State the blood parasite species.
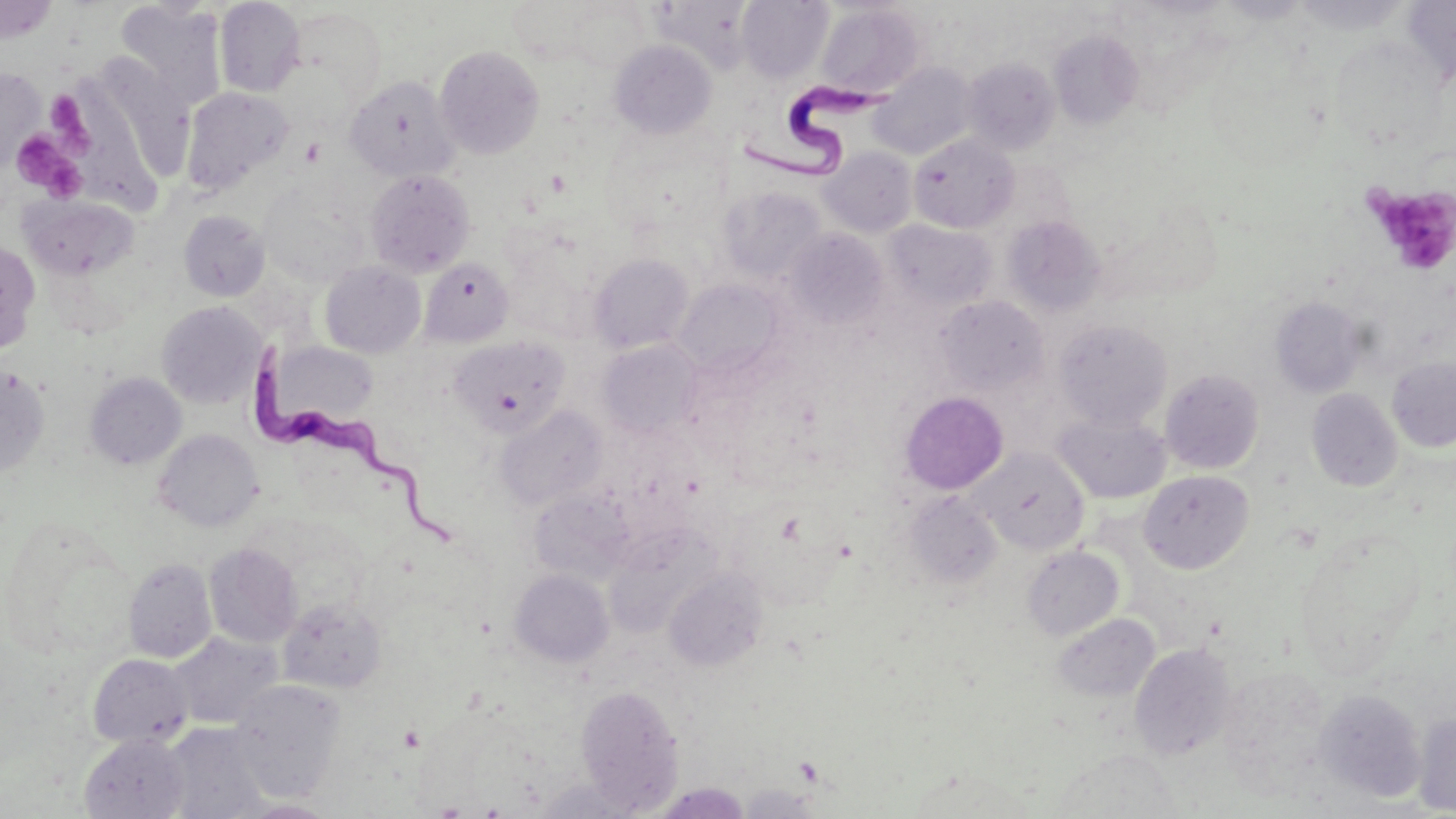

Trypanosoma brucei.

uninfected red blood cell locations = approximate bounding boxes as (x1,y1)-(x2,y2) corner pairs in pixels: (214,0)-(306,97), (737,0)-(833,82), (1292,0)-(1412,35), (1400,0)-(1456,85), (115,1)-(226,104), (1,2)-(58,43), (566,3)-(651,73), (815,3)-(925,99), (286,6)-(385,104), (1048,29)-(1143,130), (1330,36)-(1447,149), (609,40)-(717,140), (435,45)-(545,160), (964,58)-(1060,155), (870,63)-(976,160), (0,67)-(45,171), (343,75)-(462,183), (180,87)-(294,195), (909,133)-(1019,233), (819,147)-(917,238), (365,169)-(475,277), (259,186)-(370,287), (717,186)-(826,285), (20,195)-(140,280), (178,210)-(271,301), (1002,215)-(1105,315), (883,220)-(995,315), (785,229)-(889,329), (0,239)-(41,354), (501,250)-(592,343), (589,253)-(694,353), (419,257)-(514,346), (320,261)-(426,358), (673,278)-(786,379), (934,295)-(1049,396), (1270,296)-(1368,398), (156,301)-(265,408), (1054,319)-(1173,430), (450,336)-(571,439), (598,339)-(702,438), (267,342)-(381,425), (1387,357)-(1456,452), (0,365)-(51,478), (1160,368)-(1264,474), (84,372)-(186,469), (1307,388)-(1403,491), (899,391)-(1008,494), (495,404)-(607,511), (1053,412)-(1170,503), (153,428)-(262,530), (972,447)-(1089,554), (1138,470)-(1254,574), (530,489)-(636,585), (903,490)-(1003,591), (1,520)-(134,658), (602,527)-(720,637), (1294,529)-(1427,674), (204,543)-(302,648), (1023,546)-(1123,640), (123,557)-(217,663), (509,568)-(614,668), (664,568)-(767,671), (277,597)-(387,694), (1051,613)-(1160,703), (168,632)-(283,730), (1130,642)-(1237,761), (88,653)-(193,748), (1216,665)-(1333,794), (229,679)-(347,801), (576,683)-(684,811), (1315,689)-(1426,802), (1412,712)-(1456,815), (162,722)-(272,819), (80,732)-(190,818), (1048,747)-(1185,818), (907,769)-(1034,817), (735,782)-(825,818), (238,800)-(342,818)
field of view = one of a larger specimen
modality = light microscopy
magnification = 1000x
image size = 1456×819 pixels
platelet locations = approximate bounding boxes as (x1,y1)-(x2,y2) corner pairs in pixels: (45,93)-(87,138), (10,131)-(85,200), (300,137)-(326,165), (1363,183)-(1456,276)
stain = May-Grünwald-Giemsa
preparation = thin blood smear
Trypanosoma brucei locations = approximate bounding boxes as (x1,y1)-(x2,y2) corner pairs in pixels: (737,78)-(901,183), (251,340)-(462,550)